Find each cell and give its type.
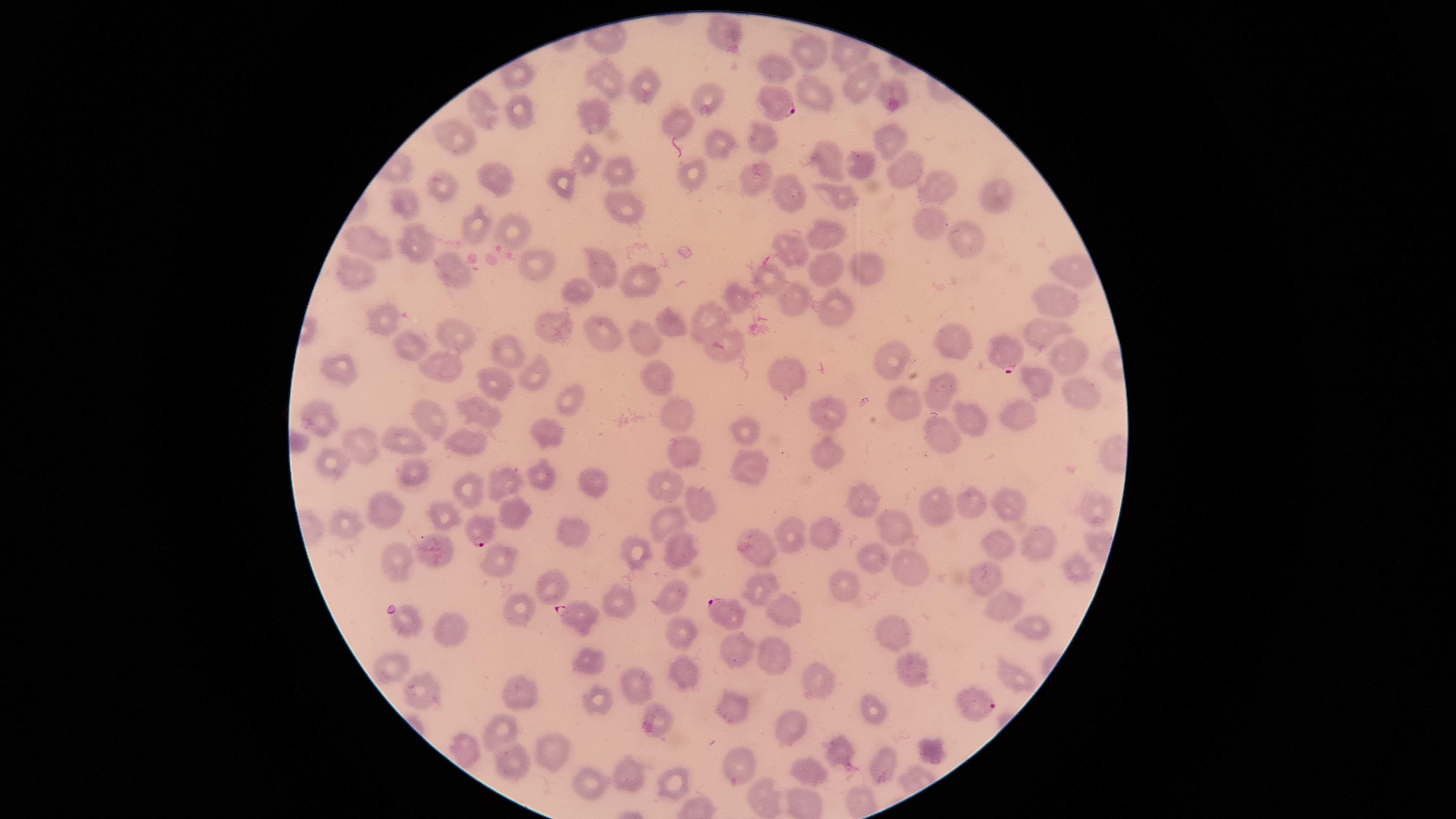

Approximate bounding boxes, in pixels from the top-left corner.
Parasitized red blood cells: (left=755, top=85, right=796, bottom=121), (left=985, top=330, right=1025, bottom=374), (left=462, top=512, right=498, bottom=547), (left=707, top=598, right=747, bottom=630), (left=554, top=600, right=600, bottom=637), (left=955, top=685, right=996, bottom=721).
Uninfected red blood cells: (left=703, top=13, right=744, bottom=55), (left=789, top=33, right=828, bottom=73), (left=830, top=33, right=871, bottom=73), (left=755, top=51, right=795, bottom=83), (left=584, top=57, right=626, bottom=98), (left=842, top=60, right=882, bottom=103), (left=624, top=66, right=662, bottom=105), (left=795, top=73, right=835, bottom=113), (left=873, top=76, right=910, bottom=112), (left=689, top=80, right=726, bottom=118), (left=464, top=86, right=501, bottom=130), (left=503, top=93, right=536, bottom=131), (left=574, top=97, right=615, bottom=136), (left=660, top=105, right=697, bottom=139), (left=433, top=118, right=478, bottom=157), (left=744, top=118, right=779, bottom=155), (left=872, top=122, right=909, bottom=162), (left=702, top=128, right=740, bottom=161), (left=808, top=139, right=846, bottom=183), (left=569, top=141, right=605, bottom=179), (left=844, top=149, right=876, bottom=181), (left=885, top=149, right=927, bottom=191), (left=600, top=153, right=639, bottom=187), (left=676, top=156, right=707, bottom=191), (left=737, top=159, right=775, bottom=197), (left=475, top=160, right=515, bottom=197), (left=544, top=166, right=578, bottom=204), (left=425, top=168, right=460, bottom=202), (left=917, top=169, right=959, bottom=207), (left=769, top=172, right=809, bottom=214), (left=978, top=177, right=1015, bottom=215), (left=811, top=181, right=860, bottom=212), (left=387, top=186, right=421, bottom=219), (left=603, top=188, right=646, bottom=226), (left=461, top=203, right=494, bottom=247), (left=912, top=204, right=949, bottom=240), (left=490, top=209, right=532, bottom=250), (left=804, top=217, right=848, bottom=252), (left=395, top=219, right=439, bottom=265), (left=945, top=219, right=986, bottom=259), (left=340, top=221, right=393, bottom=262), (left=767, top=227, right=810, bottom=271), (left=582, top=244, right=618, bottom=291), (left=514, top=246, right=559, bottom=284), (left=432, top=249, right=473, bottom=290), (left=846, top=250, right=886, bottom=286), (left=807, top=251, right=846, bottom=288), (left=333, top=252, right=377, bottom=293), (left=1047, top=253, right=1099, bottom=290), (left=751, top=257, right=791, bottom=296), (left=617, top=261, right=663, bottom=298), (left=559, top=276, right=596, bottom=304), (left=719, top=280, right=755, bottom=315), (left=775, top=280, right=811, bottom=316), (left=1031, top=281, right=1080, bottom=320), (left=814, top=286, right=855, bottom=327), (left=688, top=299, right=732, bottom=344), (left=365, top=300, right=401, bottom=338), (left=651, top=303, right=688, bottom=338), (left=534, top=310, right=574, bottom=348), (left=581, top=314, right=623, bottom=354), (left=1022, top=316, right=1075, bottom=351), (left=434, top=317, right=478, bottom=355), (left=625, top=318, right=663, bottom=358), (left=932, top=321, right=975, bottom=360), (left=704, top=326, right=746, bottom=363), (left=390, top=327, right=430, bottom=363), (left=489, top=334, right=528, bottom=370), (left=1045, top=335, right=1091, bottom=378), (left=872, top=339, right=914, bottom=381), (left=416, top=348, right=464, bottom=385), (left=318, top=352, right=359, bottom=387), (left=517, top=353, right=550, bottom=391), (left=766, top=355, right=810, bottom=396), (left=639, top=359, right=675, bottom=397), (left=1018, top=363, right=1055, bottom=402), (left=475, top=364, right=517, bottom=403), (left=921, top=371, right=959, bottom=412), (left=1061, top=376, right=1103, bottom=411), (left=553, top=382, right=587, bottom=416), (left=885, top=383, right=923, bottom=421), (left=658, top=394, right=694, bottom=435), (left=808, top=394, right=848, bottom=433), (left=453, top=395, right=503, bottom=431), (left=410, top=396, right=450, bottom=442), (left=299, top=398, right=339, bottom=438), (left=950, top=398, right=988, bottom=438), (left=997, top=398, right=1039, bottom=433), (left=922, top=411, right=963, bottom=454), (left=728, top=414, right=761, bottom=448), (left=527, top=415, right=566, bottom=451), (left=377, top=424, right=428, bottom=457), (left=442, top=424, right=496, bottom=457), (left=339, top=425, right=382, bottom=466), (left=665, top=433, right=703, bottom=469), (left=810, top=434, right=846, bottom=471), (left=313, top=446, right=352, bottom=484), (left=728, top=447, right=770, bottom=487), (left=396, top=455, right=431, bottom=490), (left=525, top=456, right=558, bottom=491), (left=485, top=466, right=525, bottom=503), (left=577, top=468, right=610, bottom=500), (left=646, top=469, right=685, bottom=504), (left=452, top=471, right=484, bottom=509), (left=844, top=480, right=882, bottom=520), (left=955, top=480, right=988, bottom=518), (left=918, top=484, right=957, bottom=527), (left=683, top=485, right=718, bottom=523), (left=989, top=486, right=1028, bottom=523), (left=365, top=488, right=406, bottom=531), (left=1074, top=488, right=1115, bottom=531), (left=497, top=495, right=534, bottom=532), (left=424, top=499, right=464, bottom=533), (left=651, top=505, right=689, bottom=544), (left=328, top=507, right=368, bottom=541), (left=874, top=507, right=913, bottom=545), (left=772, top=515, right=807, bottom=554), (left=807, top=515, right=844, bottom=551), (left=554, top=517, right=592, bottom=548), (left=1020, top=524, right=1060, bottom=564), (left=736, top=527, right=779, bottom=569), (left=979, top=528, right=1017, bottom=562), (left=661, top=530, right=701, bottom=572), (left=411, top=532, right=456, bottom=572), (left=617, top=534, right=654, bottom=572), (left=378, top=540, right=414, bottom=585), (left=855, top=540, right=893, bottom=575), (left=477, top=542, right=521, bottom=579), (left=890, top=548, right=931, bottom=587), (left=1062, top=551, right=1094, bottom=583), (left=966, top=560, right=1004, bottom=598), (left=534, top=568, right=571, bottom=607), (left=827, top=568, right=862, bottom=602), (left=740, top=572, right=782, bottom=608), (left=654, top=577, right=692, bottom=615), (left=600, top=582, right=639, bottom=619), (left=982, top=588, right=1026, bottom=622), (left=502, top=591, right=536, bottom=627), (left=764, top=594, right=804, bottom=628), (left=389, top=604, right=424, bottom=640), (left=432, top=611, right=470, bottom=649), (left=872, top=613, right=911, bottom=653), (left=1010, top=613, right=1053, bottom=642), (left=665, top=615, right=699, bottom=652), (left=719, top=631, right=758, bottom=670), (left=754, top=635, right=793, bottom=677), (left=569, top=645, right=606, bottom=675), (left=895, top=650, right=931, bottom=688), (left=371, top=651, right=412, bottom=687), (left=667, top=653, right=702, bottom=693), (left=994, top=654, right=1037, bottom=693), (left=800, top=659, right=836, bottom=701), (left=619, top=666, right=656, bottom=707), (left=401, top=670, right=443, bottom=711), (left=501, top=672, right=539, bottom=712), (left=582, top=682, right=614, bottom=717), (left=712, top=690, right=751, bottom=726), (left=860, top=692, right=890, bottom=724), (left=640, top=701, right=675, bottom=738), (left=772, top=706, right=809, bottom=748), (left=481, top=711, right=520, bottom=756), (left=533, top=732, right=573, bottom=773), (left=821, top=732, right=855, bottom=771), (left=448, top=733, right=482, bottom=771), (left=916, top=735, right=949, bottom=765), (left=492, top=742, right=530, bottom=783), (left=867, top=744, right=899, bottom=784), (left=721, top=745, right=759, bottom=787), (left=788, top=753, right=830, bottom=788), (left=611, top=754, right=646, bottom=792), (left=570, top=765, right=610, bottom=801), (left=656, top=766, right=691, bottom=802), (left=744, top=775, right=785, bottom=818), (left=846, top=783, right=880, bottom=819).
No white blood cells identified.

Smartphone photograph through the microscope eyepiece. Image is 1456×819 pixels. Single field of view. Thin blood film. Giemsa stain. Species: Plasmodium falciparum. Circular visible region.